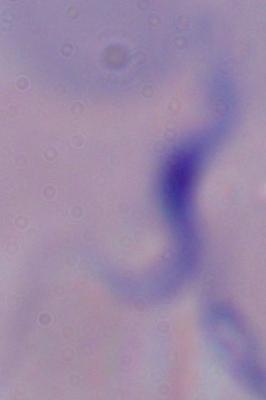

A trypanosome is seen. 1000x magnification. Photomicrograph.